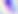
Photomicrograph. 400x magnification. Toxoplasma gondii is seen.